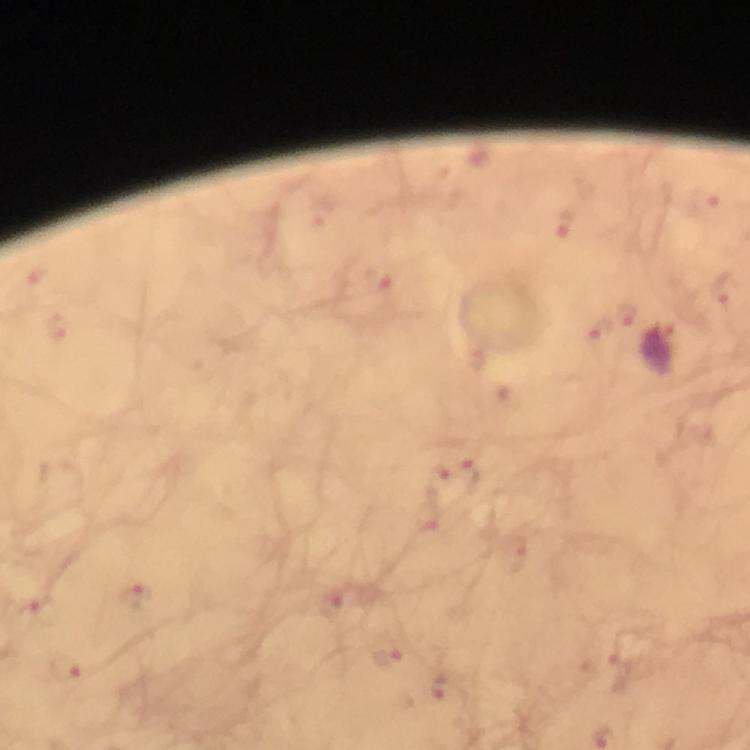
Approximate centers as (x, y) in pixels.
Summary:
  - Malaria parasite locations: (703, 198), (565, 221), (379, 280), (725, 290), (629, 314), (56, 325), (601, 328), (471, 475), (438, 480), (135, 596), (333, 604), (37, 611), (386, 658), (66, 670), (440, 686)
  - Magnification: 100x
  - Immersion oil: applied
  - Cropped from: one field of view
  - Stain: Giemsa
  - Image size: 750×750 pixels
  - Context: from a diagnostic examination for malaria
  - Preparation: thick blood smear
  - Capture: smartphone photograph through a microscope